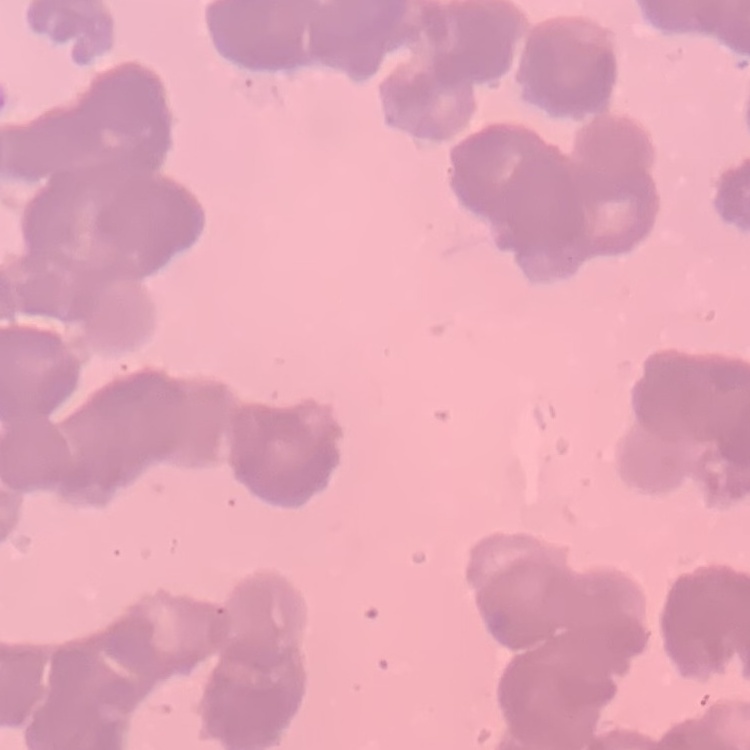

The erythrocytes show rouleaux formation. Square crop of a larger photomicrograph. Thin peripheral smear. Stained with either Field's or Giemsa.